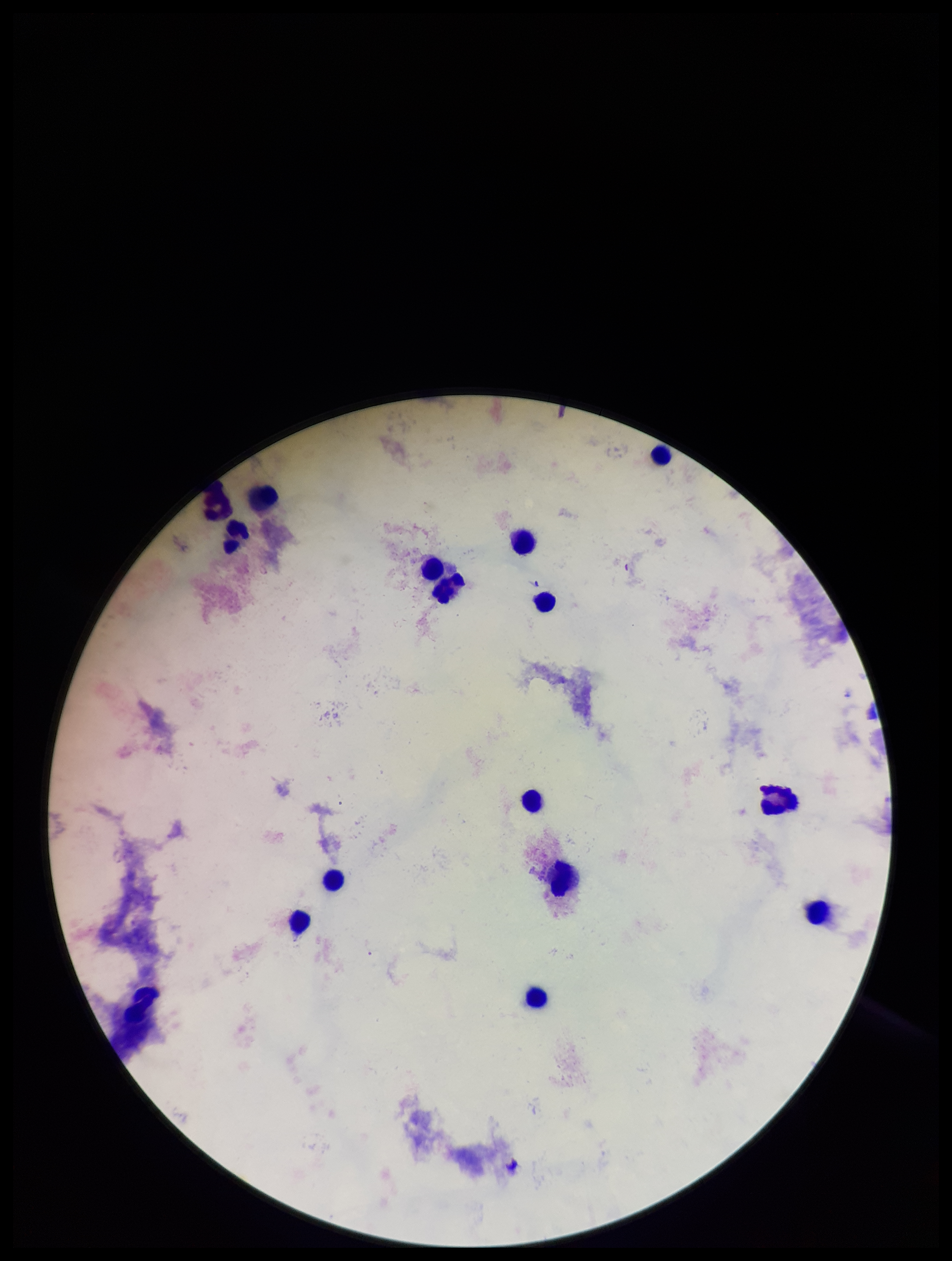
Preparation: thick smear. Plasmodium parasites: none seen. Image is 952×1261 pixels. Patient malaria status: negative. One field from this slide. Leukocyte count: 16. Stained with Giemsa. Smartphone photograph taken through the eyepiece of a microscope. Parasite count: 0.